Assess this cell for malaria.
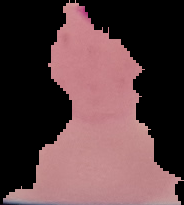

Parasitized.

Summary:
  - Preparation: thin blood smear
  - Image size: 184×205 pixels
  - Image type: cell region segmented out of the field of view; surrounding area masked to black